State the preparation type.
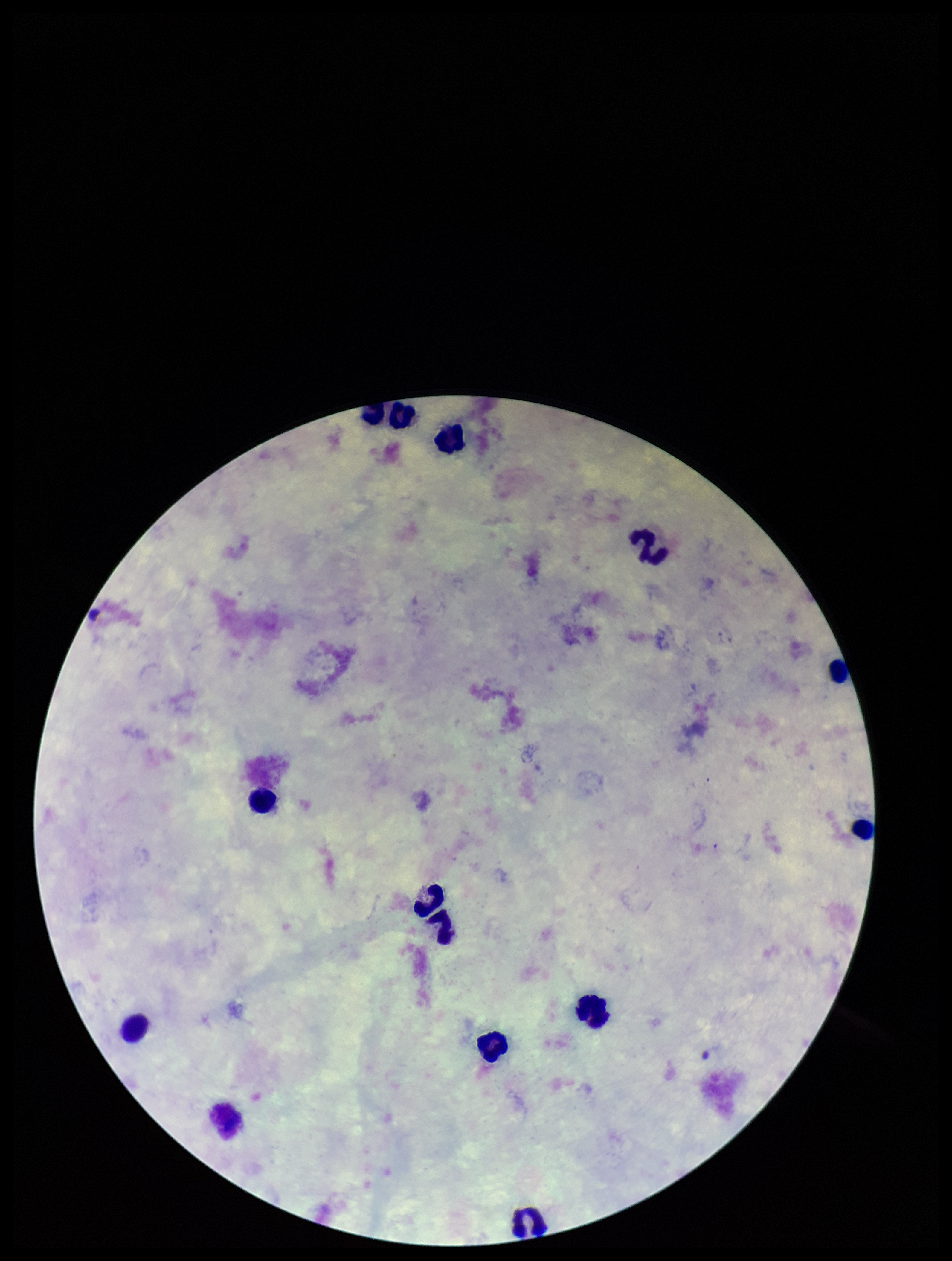
A thick smear.

Parasite count: 0. Giemsa stain. Image is 952×1261 pixels. Leukocyte count: 14. Plasmodium parasites: none identified. Smartphone photograph taken through the eyepiece of a microscope. Single field of view. Patient malaria status: negative.